Assess this cell for malaria.
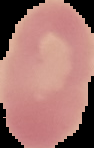

It is uninfected.

{
  "image_size": "94×148 pixels",
  "image_type": "segmented cell region on a black background",
  "preparation": "thin blood smear"
}